Report the malaria status of this cell.
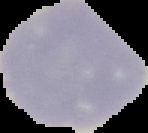
Uninfected.

Summary:
  - Image type: cell region segmented out of the field of view; surrounding area masked to black
  - Image size: 148×133 pixels
  - Preparation: thin blood film